Mark where platelets are.
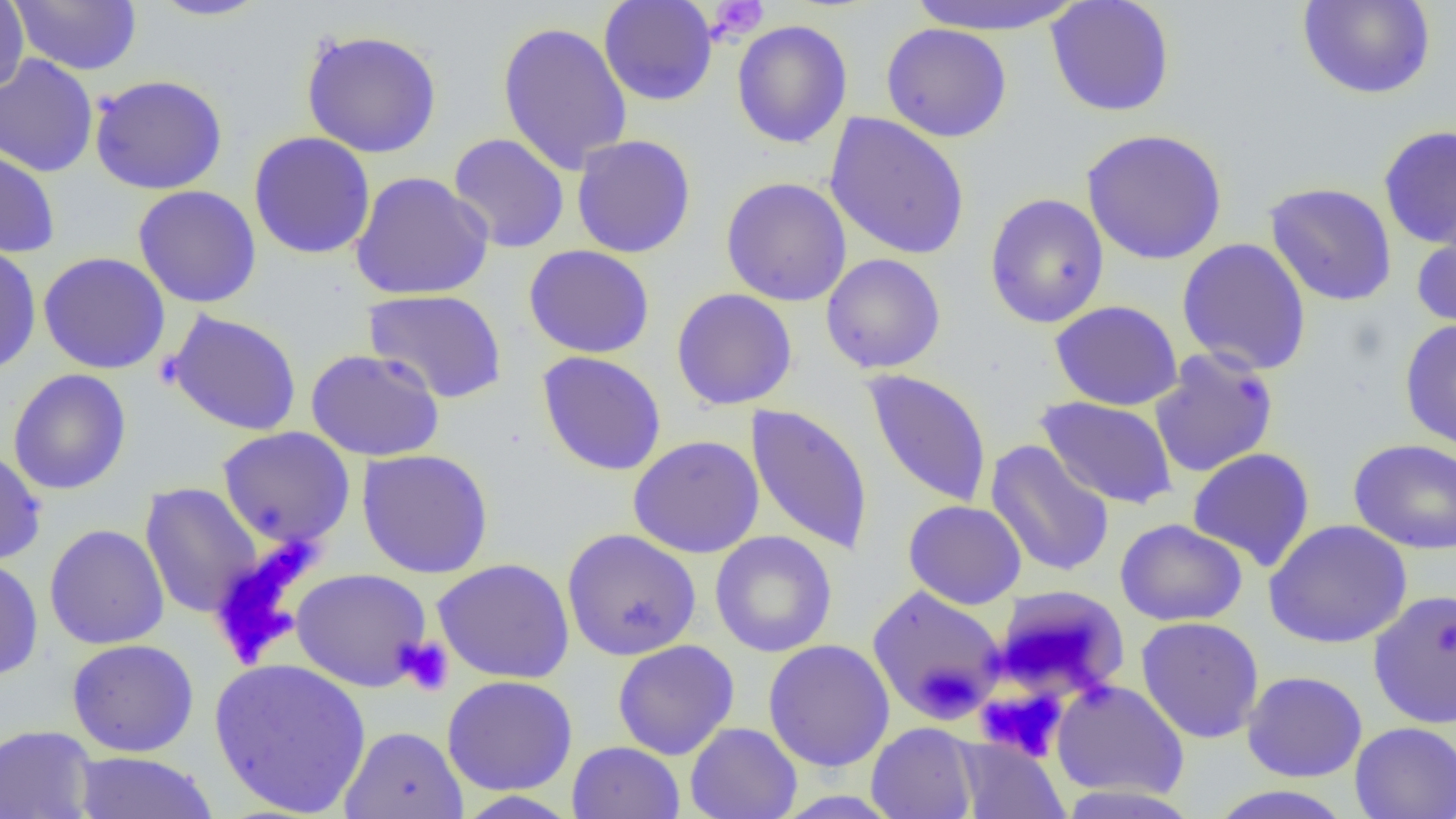

Approximate bounding boxes as (x1,y1)-(x2,y2) corner pairs in pixels.
Platelets: (705,0)-(769,42), (394,636)-(455,696), (976,687)-(1067,761).

Summary:
  - Uninfected red blood cell locations: (0,0)-(29,96), (146,0)-(272,21), (598,0)-(719,106), (907,0)-(1085,35), (1045,0)-(1176,117), (1297,0)-(1436,100), (8,1)-(142,74), (731,19)-(852,148), (497,20)-(634,174), (882,23)-(1012,142), (300,28)-(442,158), (0,53)-(99,177), (89,75)-(228,195), (824,112)-(970,260), (1377,125)-(1456,249), (1081,128)-(1228,265), (248,131)-(376,259), (447,133)-(570,253), (571,134)-(696,258), (0,146)-(60,258), (350,171)-(494,300), (720,177)-(852,306), (1264,181)-(1398,307), (132,185)-(262,308), (984,193)-(1109,328), (1412,220)-(1456,335), (1176,237)-(1312,375), (0,243)-(42,376), (523,244)-(655,358), (38,252)-(171,374), (821,253)-(946,374), (362,288)-(508,404), (671,288)-(798,410), (1050,300)-(1183,411), (165,309)-(303,436), (1399,318)-(1456,453), (305,348)-(445,462), (1149,349)-(1279,479), (536,350)-(667,476), (8,369)-(132,495), (862,369)-(993,509), (1035,396)-(1178,510), (746,403)-(874,556), (217,426)-(355,548), (628,435)-(764,558), (1348,438)-(1456,555), (985,440)-(1115,578), (0,447)-(46,566), (1187,448)-(1316,572), (357,449)-(493,578), (140,482)-(263,619), (903,500)-(1027,609), (1115,518)-(1248,626), (1263,519)-(1412,648), (44,524)-(169,649), (561,528)-(701,661), (710,530)-(837,657), (0,557)-(43,681), (433,558)-(575,684), (290,568)-(432,691), (867,585)-(1008,723), (1368,588)-(1456,729), (1136,616)-(1265,743), (67,638)-(199,757), (762,639)-(895,771), (612,640)-(739,760), (208,657)-(372,817), (1241,670)-(1368,782), (442,675)-(578,796), (1051,679)-(1190,801), (684,722)-(802,819), (866,722)-(978,819), (1350,722)-(1456,819), (0,724)-(99,819), (339,725)-(468,819), (956,737)-(1069,819), (567,741)-(685,819), (70,751)-(218,818), (1053,784)-(1205,818), (1204,785)-(1356,819), (452,790)-(582,818)
  - Slide-level diagnosis: negative for blood parasites
  - Magnification: 1000x
  - Modality: optical microscopy
  - Field of view: one of a larger specimen
  - Preparation: thin blood smear
  - Image size: 1456×819 pixels